Locate and identify every blood parasite.
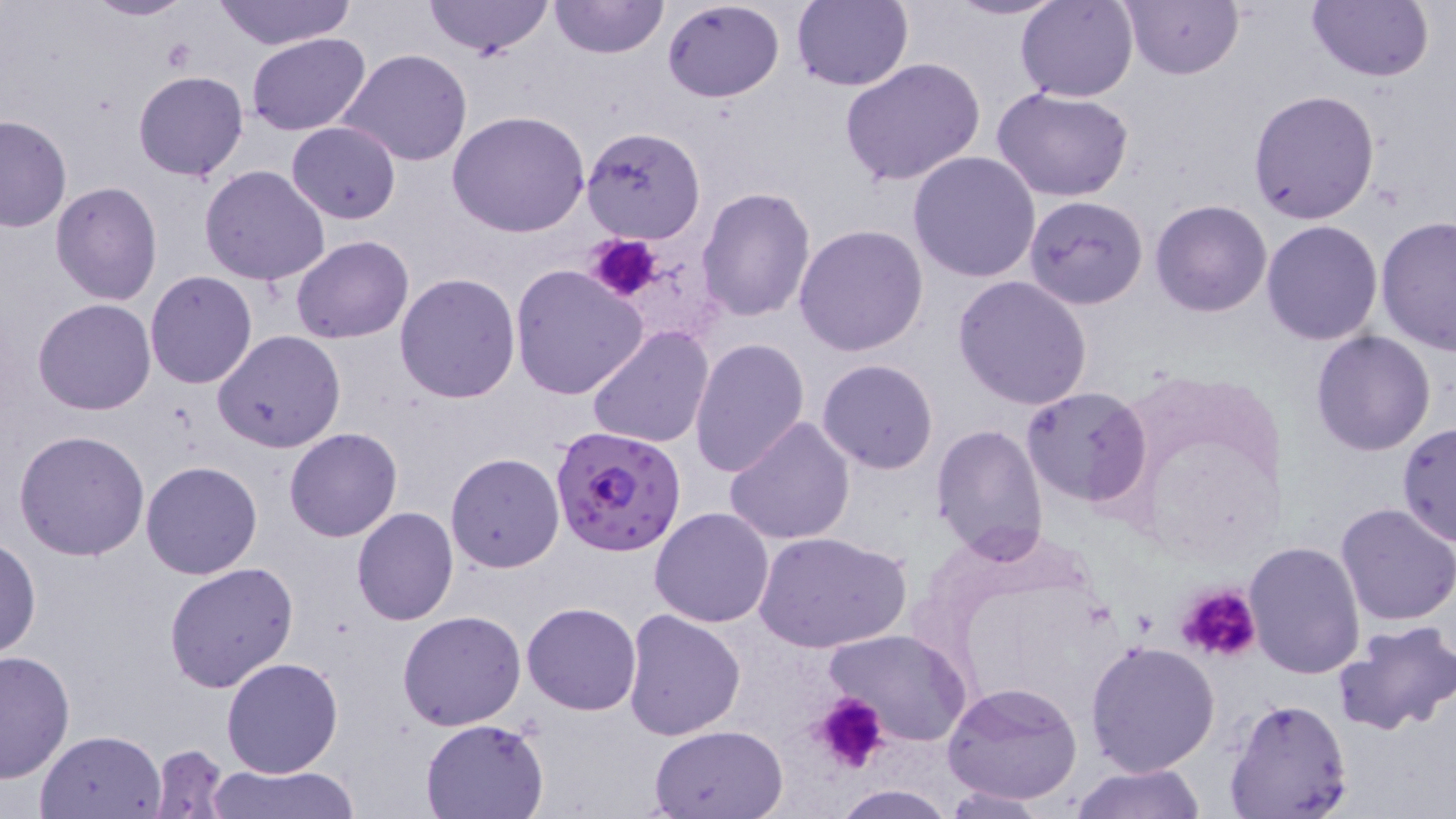
Approximate bounding boxes as named x1/y1/x2/y2 corners in pixels.
Plasmodium falciparum-infected red blood cells: (x1=551, y1=422, x2=686, y2=558).
No Plasmodium ovale, Plasmodium malariae, Plasmodium vivax, Babesia divergens, or Trypanosoma brucei observed.

slide-level diagnosis = Plasmodium falciparum
image size = 1456×819 pixels
platelet locations = approximate bounding boxes as named x1/y1/x2/y2 corners in pixels: (x1=585, y1=232, x2=663, y2=306), (x1=1175, y1=583, x2=1263, y2=666), (x1=812, y1=692, x2=889, y2=775)
field of view = single
uninfected red blood cell locations = approximate bounding boxes as named x1/y1/x2/y2 corners in pixels: (x1=82, y1=0, x2=198, y2=22), (x1=209, y1=0, x2=357, y2=49), (x1=423, y1=0, x2=553, y2=59), (x1=548, y1=0, x2=670, y2=60), (x1=661, y1=0, x2=785, y2=103), (x1=792, y1=0, x2=912, y2=92), (x1=946, y1=0, x2=1064, y2=21), (x1=1120, y1=0, x2=1241, y2=79), (x1=1307, y1=0, x2=1434, y2=83), (x1=1016, y1=1, x2=1140, y2=102), (x1=245, y1=33, x2=371, y2=135), (x1=340, y1=50, x2=474, y2=167), (x1=840, y1=56, x2=988, y2=188), (x1=132, y1=69, x2=249, y2=182), (x1=994, y1=88, x2=1134, y2=203), (x1=1246, y1=88, x2=1380, y2=226), (x1=446, y1=111, x2=591, y2=238), (x1=0, y1=114, x2=72, y2=233), (x1=287, y1=121, x2=400, y2=225), (x1=581, y1=125, x2=706, y2=244), (x1=908, y1=151, x2=1043, y2=283), (x1=199, y1=165, x2=330, y2=285), (x1=50, y1=181, x2=163, y2=305), (x1=697, y1=186, x2=816, y2=322), (x1=1023, y1=195, x2=1150, y2=310), (x1=1151, y1=200, x2=1272, y2=317), (x1=1376, y1=217, x2=1456, y2=356), (x1=1261, y1=220, x2=1383, y2=345), (x1=794, y1=223, x2=928, y2=357), (x1=292, y1=235, x2=414, y2=345), (x1=509, y1=264, x2=649, y2=401), (x1=145, y1=270, x2=258, y2=389), (x1=394, y1=273, x2=521, y2=403), (x1=951, y1=274, x2=1095, y2=411), (x1=32, y1=298, x2=156, y2=416), (x1=587, y1=326, x2=713, y2=447), (x1=214, y1=330, x2=346, y2=453), (x1=1311, y1=331, x2=1437, y2=457), (x1=689, y1=338, x2=811, y2=478), (x1=817, y1=359, x2=940, y2=474), (x1=1021, y1=386, x2=1151, y2=505), (x1=724, y1=416, x2=856, y2=545), (x1=1397, y1=420, x2=1456, y2=547), (x1=930, y1=423, x2=1048, y2=561), (x1=284, y1=427, x2=403, y2=542), (x1=14, y1=430, x2=149, y2=560), (x1=444, y1=453, x2=564, y2=574), (x1=140, y1=460, x2=262, y2=579), (x1=1334, y1=501, x2=1456, y2=624), (x1=649, y1=506, x2=776, y2=626), (x1=352, y1=507, x2=459, y2=625), (x1=752, y1=530, x2=911, y2=655), (x1=0, y1=535, x2=40, y2=661), (x1=1243, y1=540, x2=1366, y2=683), (x1=164, y1=562, x2=298, y2=692), (x1=520, y1=603, x2=642, y2=716), (x1=622, y1=608, x2=746, y2=740), (x1=398, y1=610, x2=526, y2=730), (x1=1331, y1=620, x2=1456, y2=737), (x1=826, y1=628, x2=973, y2=745), (x1=1084, y1=640, x2=1220, y2=776), (x1=0, y1=650, x2=75, y2=784), (x1=221, y1=655, x2=345, y2=777), (x1=941, y1=679, x2=1084, y2=807), (x1=1224, y1=697, x2=1352, y2=819), (x1=420, y1=718, x2=548, y2=818), (x1=650, y1=724, x2=788, y2=817), (x1=35, y1=730, x2=167, y2=819), (x1=147, y1=743, x2=230, y2=817), (x1=1067, y1=762, x2=1208, y2=818), (x1=203, y1=763, x2=359, y2=819), (x1=941, y1=783, x2=1052, y2=817), (x1=833, y1=784, x2=954, y2=818)
modality = optical microscopy
magnification = 1000x
preparation = thin blood film
stain = May-Grünwald-Giemsa